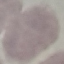
{
  "result": "no malaria parasites seen",
  "capture": "smartphone through the microscope eyepiece",
  "stain": "Giemsa",
  "preparation": "thin blood smear",
  "image_type": "cell patch, automatically extracted from a larger field of view and resized to 64 × 64 pixels"
}